Name the cell type shown.
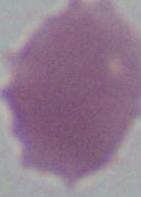
An erythrocyte.

Micrograph. 1000x magnification.